Name the cell type shown.
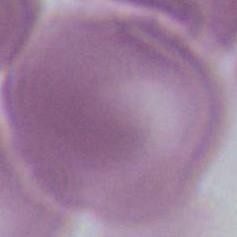

An erythrocyte.

Captured at 1000x magnification. Photomicrograph.